Identify the preparation type.
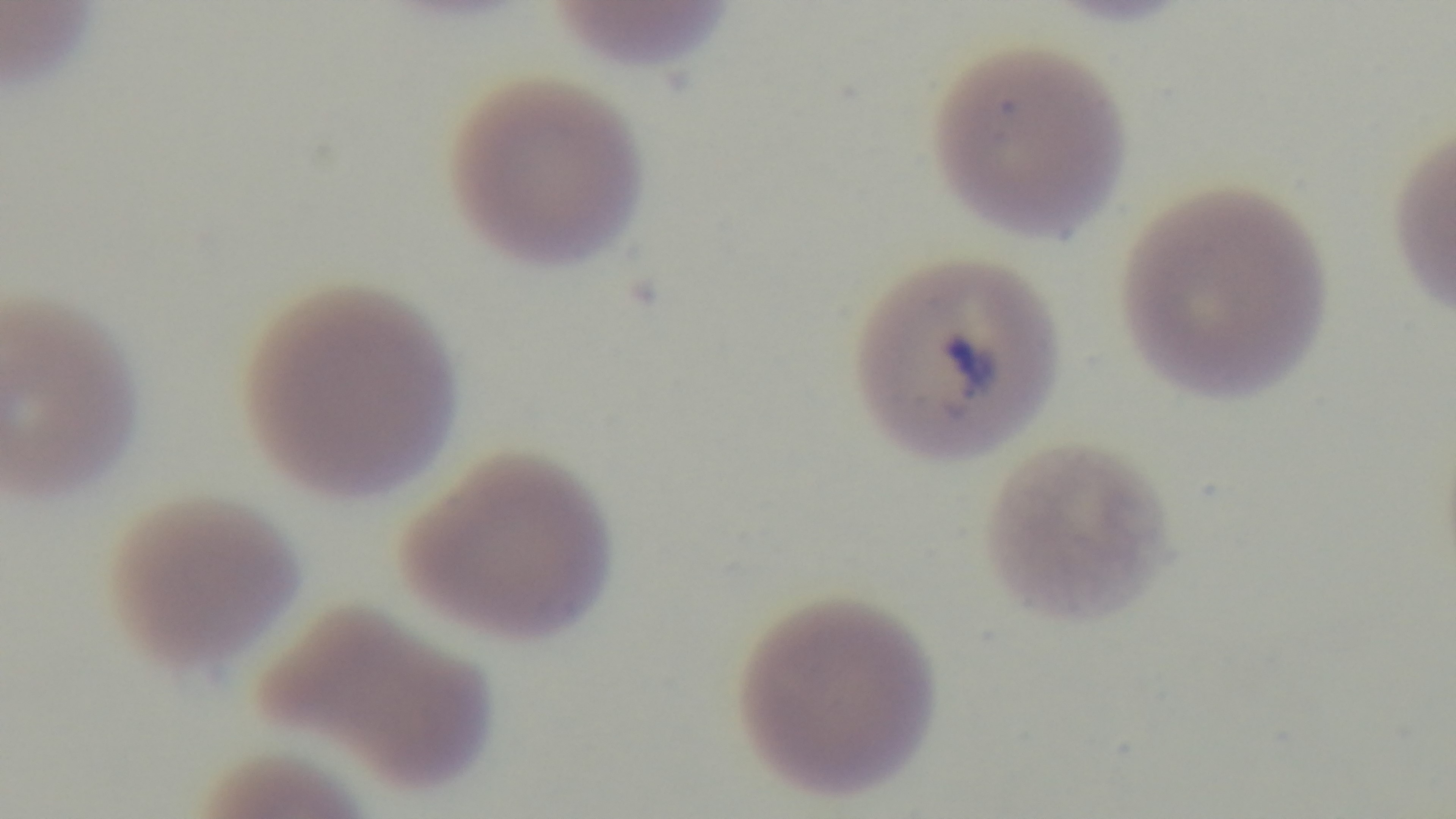

Thin.

Summary:
  - Field of view: one from the slide
  - Modality: light microscopy
  - Malaria status: positive
  - Stain: Giemsa
  - Objective: 100x oil immersion
  - Capture: mounted 4K digital camera